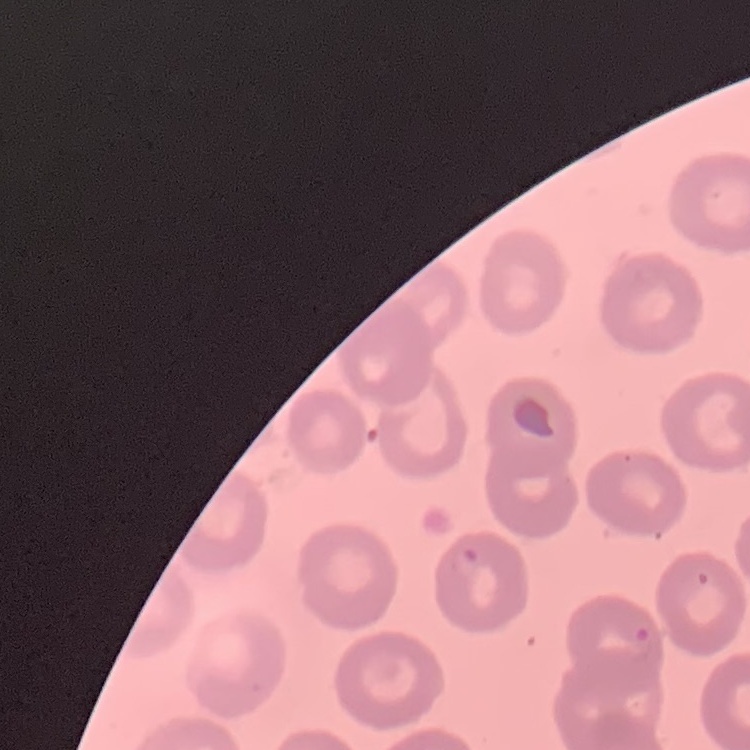

Summary:
  - Red blood cell morphology: no rouleaux formation
  - Stain: Field's or Giemsa
  - Preparation: thin peripheral smear
  - Image type: one tile cut from a larger photomicrograph